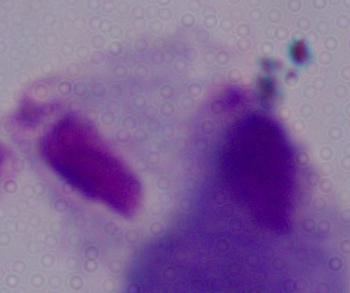

Captured at 1000x magnification. Micrograph. A trichomonad is seen.